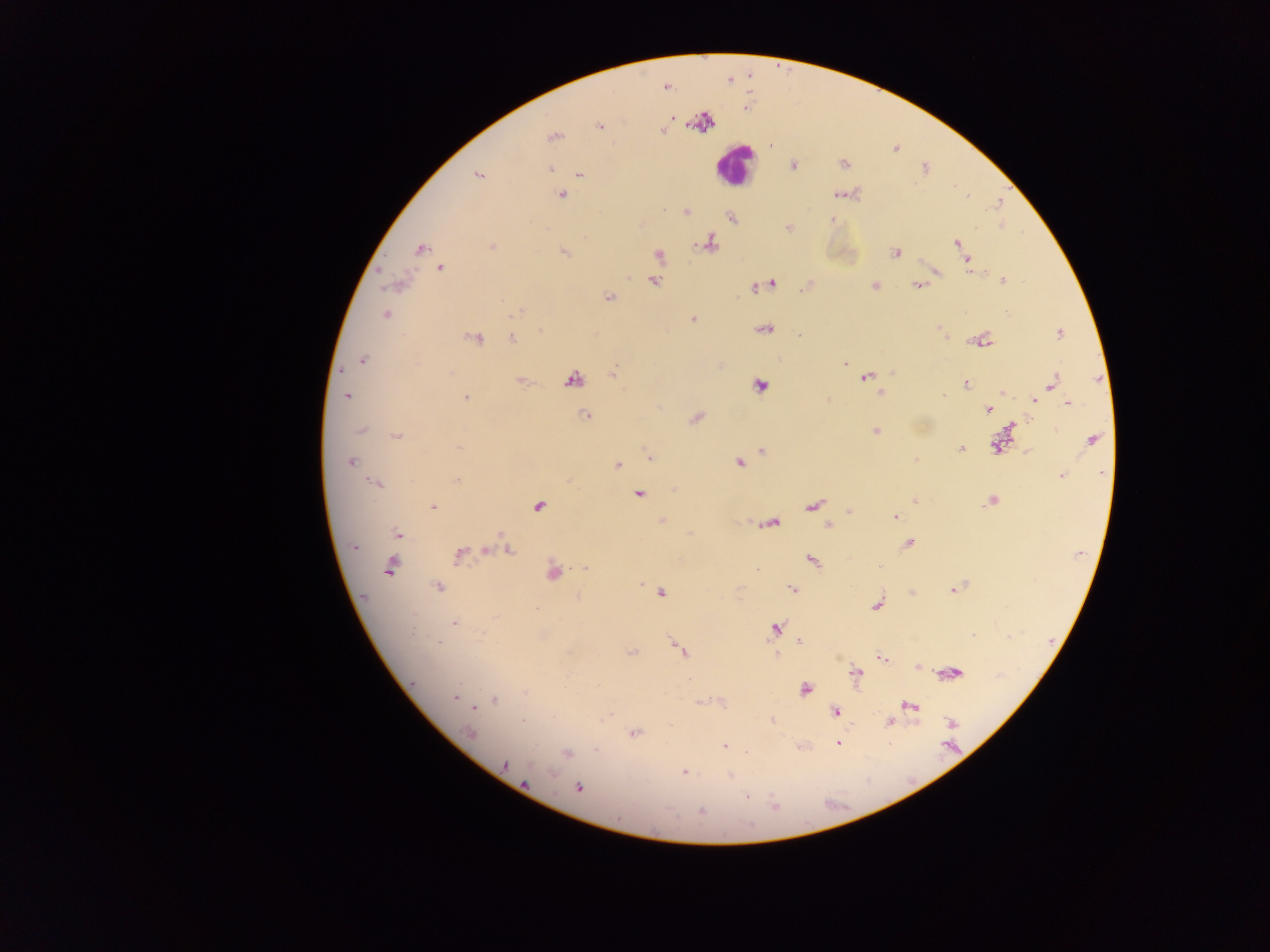

Approximate centers as x y in pixels.
Summary:
  - Leukocyte locations: 734 165
  - Malaria parasite locations: 666 87; 744 109; 600 127; 662 130; 554 135; 771 144; 843 164; 793 165; 549 169; 478 175; 580 175; 561 195; 838 195; 967 197; 686 212; 832 219; 789 228; 710 243; 957 243; 492 247; 420 248; 564 252; 895 253; 659 255; 968 261; 441 268; 971 271; 937 272; 1002 280; 654 281; 773 283; 918 285; 875 286; 754 288; 608 297; 517 311; 385 315; 692 319; 764 329; 540 332; 1059 333; 799 334; 476 337; 512 339; 982 341; 363 359; 844 364; 892 372; 612 373; 866 378; 573 380; 520 381; 965 383; 1053 383; 759 386; 1003 393; 881 394; 347 396; 943 396; 1038 396; 465 398; 1034 401; 1068 403; 989 410; 586 415; 696 418; 1012 425; 362 430; 875 431; 397 436; 1092 439; 997 446; 458 447; 960 449; 762 451; 649 458; 915 460; 351 461; 739 463; 617 465; 1062 476; 457 480; 376 484; 638 494; 914 501; 992 501; 813 505; 433 507; 538 507; 849 512; 895 517; 663 521; 772 523; 828 525; 397 533; 501 534; 908 543; 354 547; 486 550; 509 551; 459 555; 812 561; 390 567; 880 567; 585 568; 757 570; 553 572; 641 584; 439 587; 791 589; 953 589; 662 593; 577 598; 876 605; 535 608; 495 617; 454 623; 776 628; 412 632; 973 636; 799 641; 438 642; 680 649; 632 652; 776 655; 883 658; 917 667; 856 673; 954 673; 689 679; 805 689; 525 692; 455 697; 495 701; 910 706; 475 708; 834 711; 523 721; 771 721; 890 722; 951 723; 634 732; 468 733; 838 743; 724 747; 566 752; 505 764; 684 772; 552 774; 730 775; 527 783; 579 787; 747 795; 773 806; 701 811
  - Image size: 1270×952 pixels
  - Country: Ghana
  - Preparation: thick blood film
  - Field of view: single
  - Capture: mobile-phone photograph through a microscope